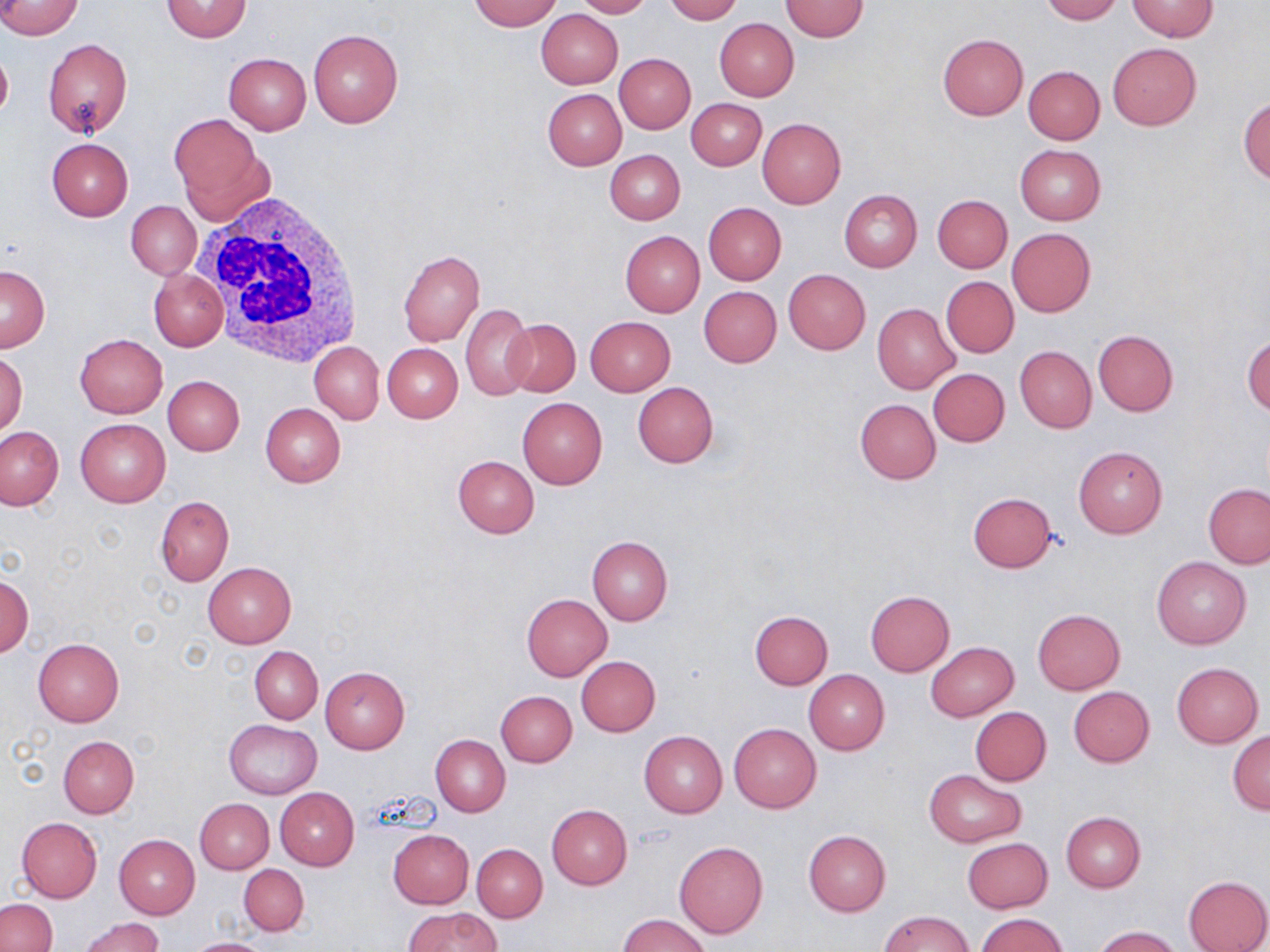
Approximate bounding boxes as (x1, y1, x2, y2) in pixels. White blood cell locations: (193, 192, 370, 366). Uninfected red blood cell locations: (0, 0, 84, 40), (161, 0, 252, 42), (469, 0, 562, 30), (572, 0, 652, 18), (663, 0, 741, 23), (1041, 0, 1121, 24), (781, 1, 869, 41), (1126, 1, 1218, 41), (535, 9, 622, 89), (715, 18, 799, 101), (307, 29, 402, 128), (938, 33, 1028, 119), (42, 38, 132, 138), (1108, 42, 1201, 130), (0, 45, 12, 123), (224, 53, 311, 134), (615, 54, 695, 133), (1023, 66, 1105, 145), (543, 88, 626, 170), (1238, 96, 1269, 183), (688, 98, 766, 170), (171, 114, 264, 204), (757, 118, 846, 208), (46, 138, 132, 220), (1015, 145, 1105, 225), (605, 150, 684, 224), (839, 189, 922, 271), (932, 195, 1013, 273), (126, 201, 200, 280), (703, 202, 786, 284), (1007, 228, 1095, 317), (621, 231, 704, 316), (398, 249, 484, 345), (0, 265, 50, 351), (148, 269, 227, 351), (784, 269, 871, 354), (941, 277, 1018, 357), (698, 286, 782, 367), (460, 303, 534, 400), (872, 303, 960, 394), (585, 316, 676, 396), (503, 318, 581, 398), (1092, 330, 1179, 416), (75, 334, 168, 417), (1244, 336, 1270, 417), (309, 341, 383, 423), (382, 343, 463, 422), (1015, 345, 1097, 432), (0, 352, 27, 435), (928, 368, 1009, 446), (163, 375, 244, 455), (632, 381, 719, 468), (517, 398, 607, 490), (855, 398, 940, 484), (260, 403, 346, 486), (76, 419, 169, 506), (0, 425, 66, 511), (1073, 446, 1168, 539), (452, 455, 539, 538), (1203, 483, 1270, 568), (967, 492, 1057, 573), (155, 496, 234, 585), (172, 510, 265, 616), (587, 536, 673, 625), (1152, 557, 1251, 650), (203, 562, 297, 648), (0, 574, 32, 657), (865, 591, 955, 676), (522, 593, 613, 682), (1033, 609, 1125, 694), (750, 611, 833, 689), (33, 637, 124, 726), (926, 642, 1019, 721), (250, 647, 322, 723), (577, 656, 660, 736), (1172, 662, 1263, 747), (320, 667, 410, 753), (803, 670, 890, 755), (1068, 686, 1155, 767), (496, 691, 576, 766), (971, 707, 1051, 785), (224, 719, 321, 799), (729, 723, 821, 813), (1228, 730, 1270, 814), (639, 731, 727, 817), (431, 734, 511, 816), (58, 735, 139, 818), (924, 770, 1026, 846), (276, 788, 359, 871), (195, 798, 273, 874), (547, 805, 632, 889), (1060, 811, 1146, 892), (17, 817, 102, 903), (389, 829, 474, 908), (802, 830, 890, 917), (114, 835, 200, 919), (961, 837, 1053, 912), (674, 841, 768, 939), (472, 844, 548, 922), (239, 864, 309, 935), (1183, 875, 1269, 952), (0, 899, 56, 952), (405, 908, 499, 952), (879, 911, 975, 952), (976, 913, 1069, 952), (620, 914, 711, 952), (79, 916, 165, 952), (1092, 926, 1184, 952), (185, 938, 273, 952). Slide-level diagnosis: negative for blood parasites. 1000x magnification. Thin blood film. One field of a larger specimen. Light microscopy. May-Grünwald-Giemsa stain. Image is 1270×952 pixels.